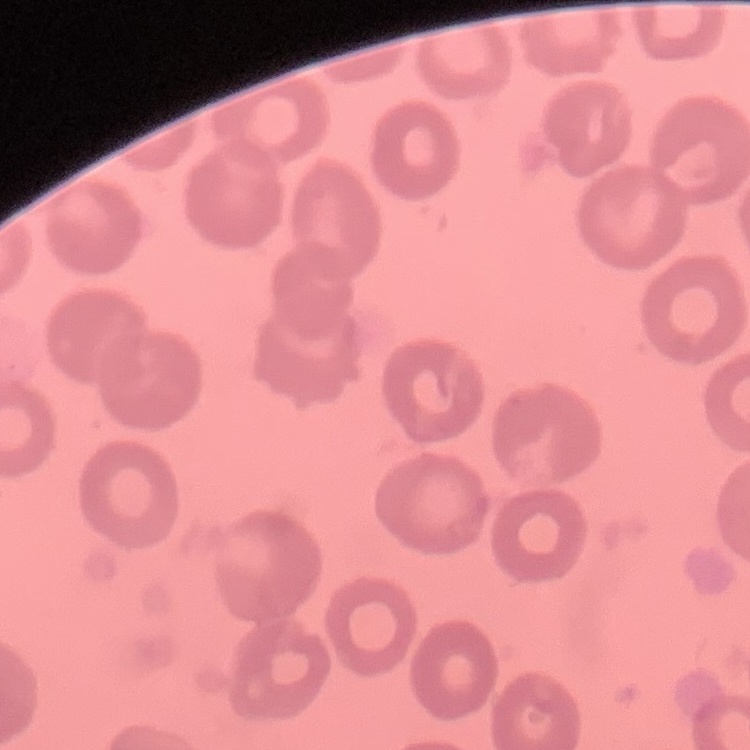 The erythrocytes show no rouleaux formation. One tile cut from a larger photomicrograph. Field's or Giemsa stain. Thin blood smear.